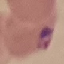
{
  "malaria_status": "parasitized",
  "capture": "smartphone through the microscope eyepiece",
  "image_type": "cell patch, automatically extracted from a larger field of view and resized to 64 × 64 pixels",
  "preparation": "thin blood film",
  "stain": "Giemsa"
}